Report the malaria status of this cell.
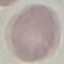

It is uninfected.

stain = Giemsa
image type = automatically extracted cell patch, resized to 64 × 64 pixels
preparation = thin smear
capture = smartphone camera at the microscope eyepiece